Locate and identify every blood parasite.
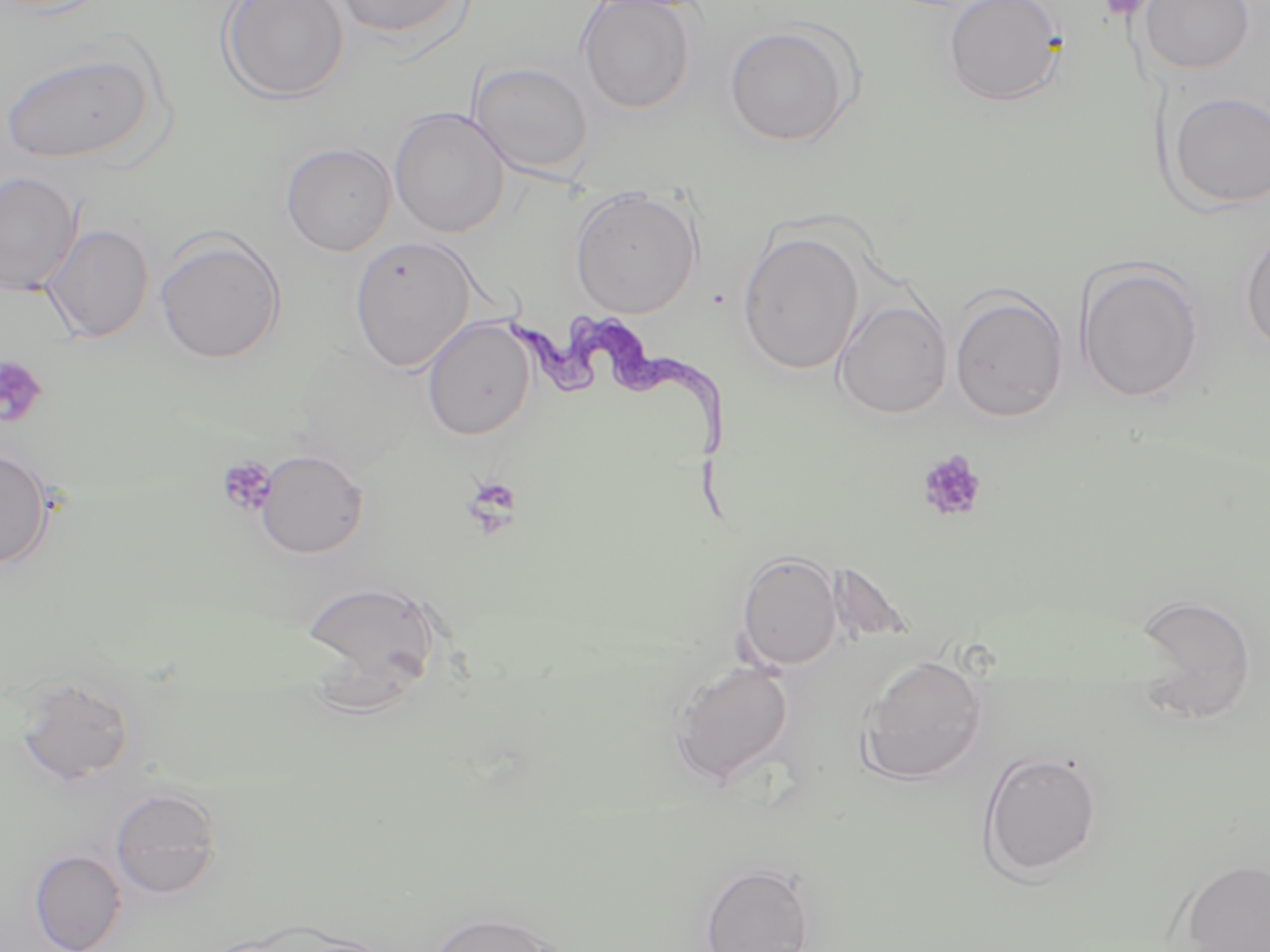

Approximate bounding boxes as (x1,y1)-(x2,y2) corner pairs in pixels.
Trypanosoma brucei: (509,310)-(746,527).
No Plasmodium falciparum, Plasmodium ovale, Plasmodium malariae, Plasmodium vivax, or Babesia divergens observed.

slide-level diagnosis = Trypanosoma brucei
stain = May-Grünwald-Giemsa
image size = 1270×952 pixels
uninfected red blood cell locations = approximate bounding boxes as (x1,y1)-(x2,y2) corner pairs in pixels: (218,0)-(350,105), (329,0)-(468,39), (942,0)-(1067,108), (1138,0)-(1255,75), (576,1)-(696,114), (724,25)-(857,147), (2,50)-(157,164), (468,61)-(593,178), (1164,90)-(1270,211), (389,107)-(510,238), (280,142)-(397,256), (0,171)-(82,295), (569,187)-(702,319), (42,224)-(155,343), (1241,225)-(1270,358), (154,231)-(286,365), (737,231)-(865,375), (349,236)-(477,373), (1074,260)-(1205,404), (948,289)-(1069,423), (833,299)-(952,419), (421,317)-(535,441), (0,445)-(54,570), (256,449)-(369,558), (735,550)-(843,672), (299,578)-(443,697), (1130,593)-(1258,723), (860,653)-(988,785), (670,660)-(795,788), (14,675)-(135,785), (978,749)-(1103,883), (110,787)-(222,899), (28,848)-(126,952), (1177,859)-(1270,951), (699,861)-(817,952), (425,908)-(567,952)
magnification = 1000x
modality = optical microscopy
field of view = single
platelet locations = approximate bounding boxes as (x1,y1)-(x2,y2) corner pairs in pixels: (1098,0)-(1154,21), (0,355)-(48,428), (916,449)-(988,524), (216,457)-(277,517), (461,475)-(523,534)
preparation = thin blood film